Give the preparation type.
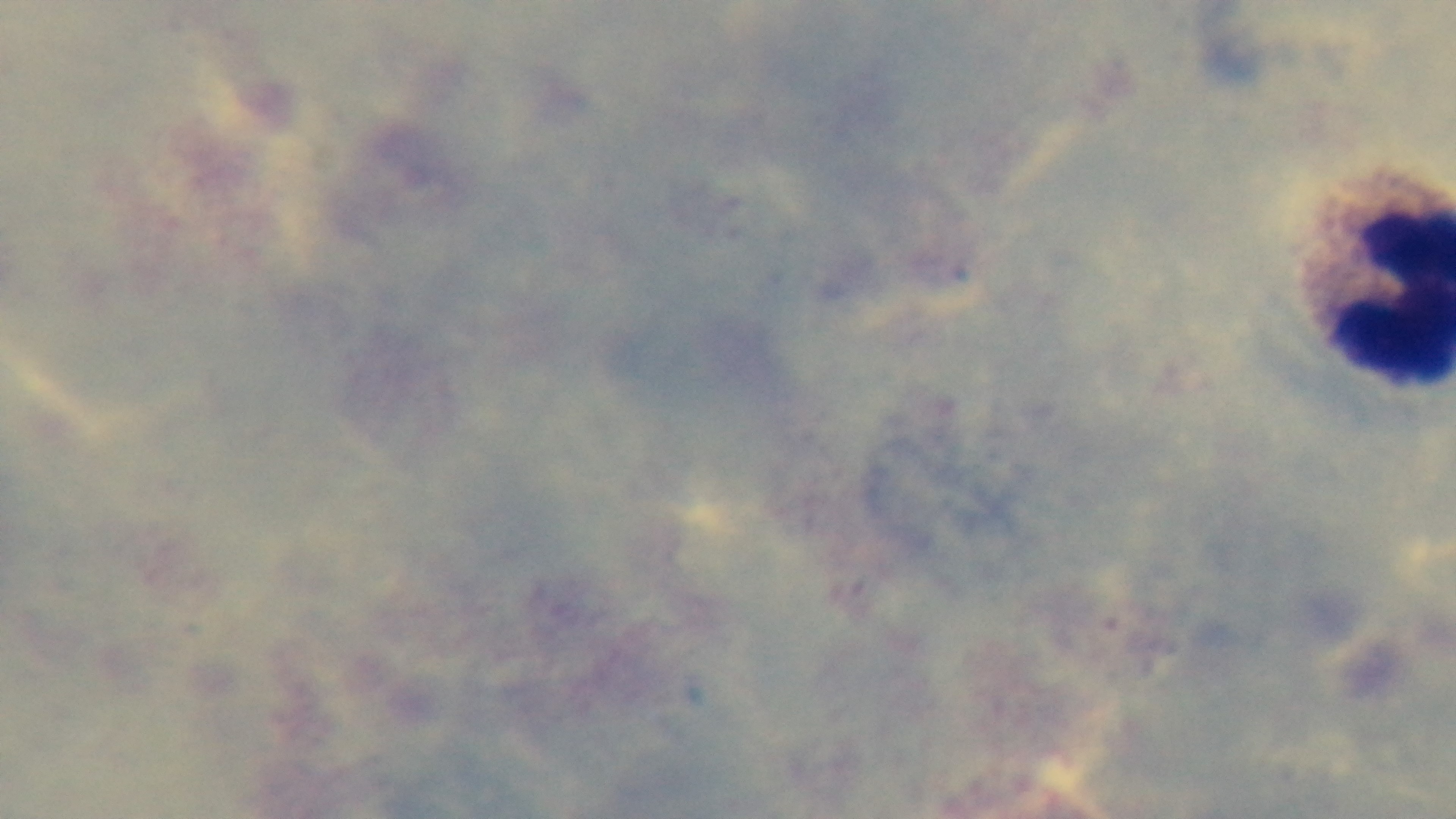

Thick.

Summary:
  - Field of view: single
  - Objective: 100x oil immersion
  - Modality: light microscopy
  - Malaria status: negative
  - Capture: mounted 4K digital camera
  - Stain: Giemsa